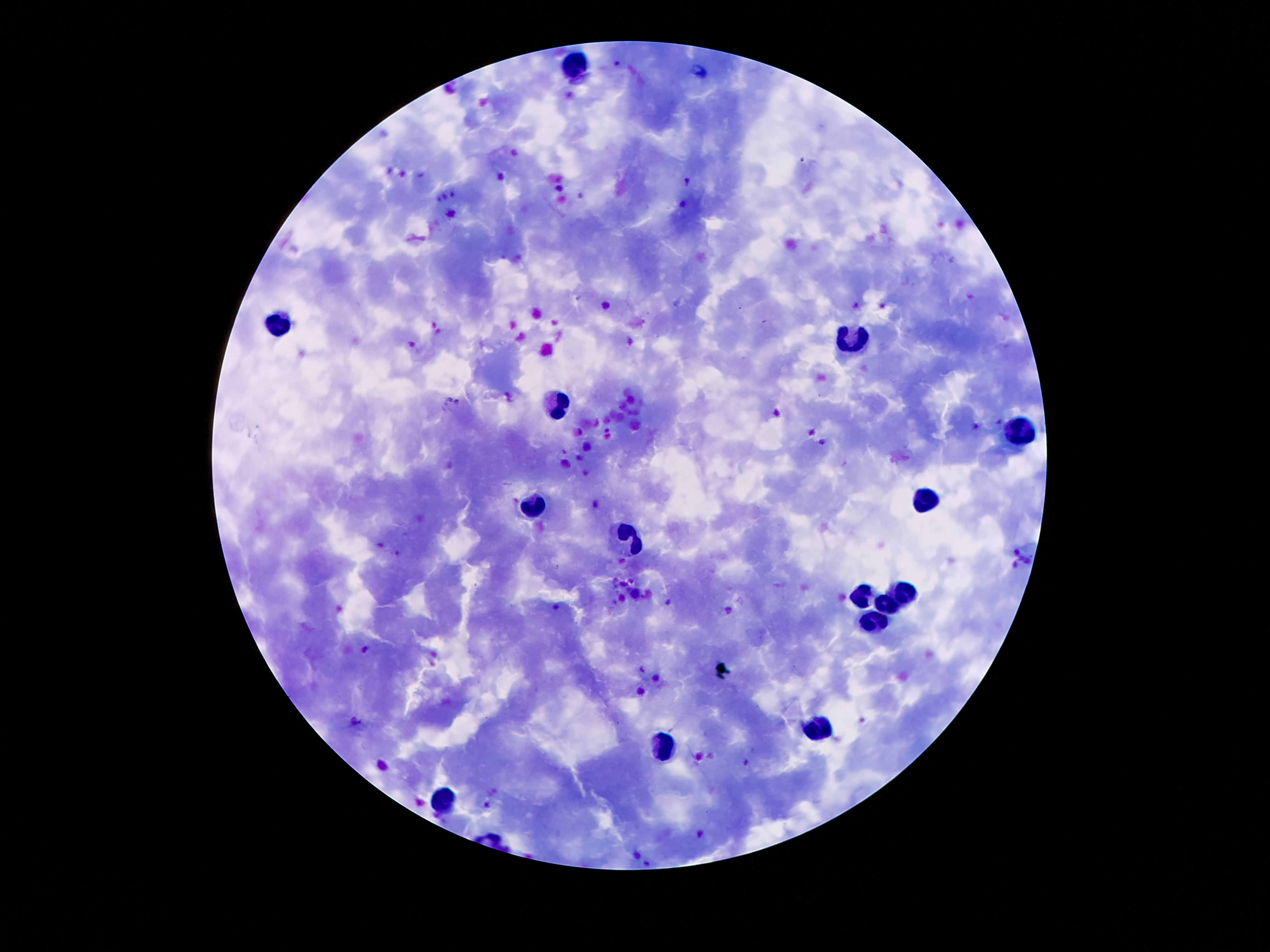 Approximate object centers, in pixels from the top-left corner. Plasmodium parasite locations: (x=687, y=181), (x=605, y=305), (x=366, y=650). Leukocyte locations: (x=575, y=61), (x=276, y=319), (x=854, y=337), (x=560, y=406), (x=1014, y=429), (x=928, y=500), (x=532, y=504), (x=630, y=539), (x=905, y=591), (x=862, y=595), (x=887, y=603), (x=872, y=618), (x=815, y=728), (x=663, y=746), (x=442, y=802). 100x magnification. Giemsa-stained preparation. Thick blood smear. Patient malaria status: infected with Plasmodium falciparum. Photographed through the microscope eyepiece with a smartphone camera. Image is 1270×952 pixels. One field from this slide.